Name the cell type shown.
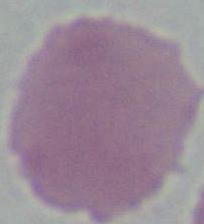
This is an erythrocyte.

magnification = 1000x
modality = micrograph